Locate every Plasmodium falciparum-infected red blood cell.
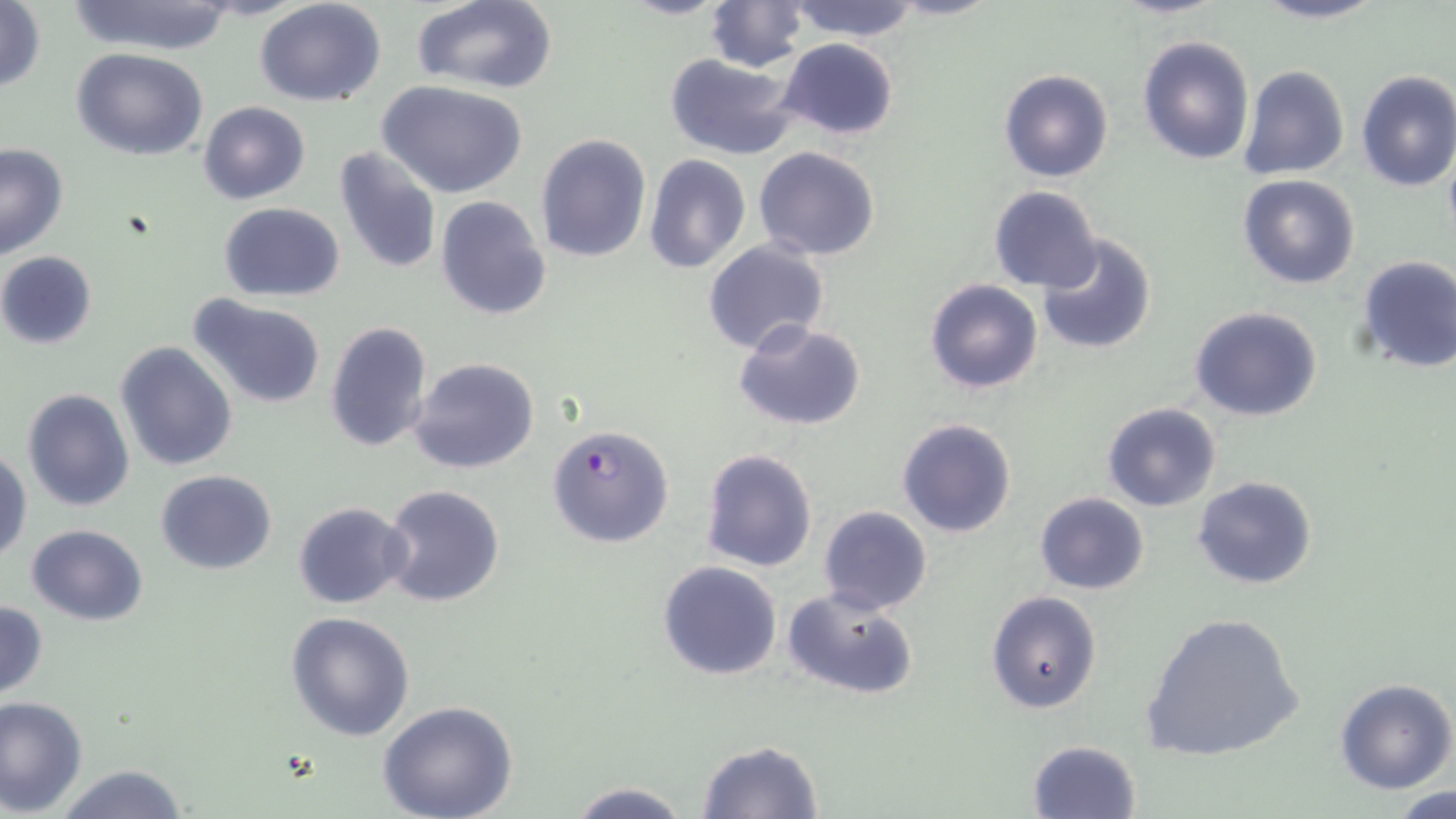

Approximate bounding boxes as named x1/y1/x2/y2 corners in pixels.
Plasmodium falciparum-infected red blood cells: (x1=547, y1=424, x2=675, y2=548).

Summary:
  - Uninfected red blood cell locations: (x1=65, y1=0, x2=241, y2=55), (x1=253, y1=0, x2=387, y2=107), (x1=410, y1=0, x2=559, y2=93), (x1=618, y1=0, x2=731, y2=19), (x1=787, y1=0, x2=922, y2=41), (x1=1113, y1=0, x2=1226, y2=19), (x1=1251, y1=0, x2=1387, y2=25), (x1=1, y1=1, x2=48, y2=94), (x1=704, y1=1, x2=809, y2=72), (x1=1137, y1=34, x2=1255, y2=167), (x1=777, y1=38, x2=901, y2=142), (x1=71, y1=47, x2=210, y2=161), (x1=664, y1=53, x2=803, y2=161), (x1=1238, y1=65, x2=1350, y2=181), (x1=998, y1=68, x2=1114, y2=184), (x1=1354, y1=69, x2=1456, y2=192), (x1=378, y1=80, x2=528, y2=198), (x1=198, y1=100, x2=310, y2=204), (x1=535, y1=132, x2=652, y2=263), (x1=0, y1=144, x2=69, y2=261), (x1=332, y1=144, x2=442, y2=276), (x1=753, y1=147, x2=881, y2=261), (x1=644, y1=155, x2=750, y2=274), (x1=1239, y1=175, x2=1361, y2=290), (x1=988, y1=185, x2=1104, y2=293), (x1=433, y1=196, x2=552, y2=321), (x1=218, y1=202, x2=345, y2=300), (x1=1034, y1=233, x2=1159, y2=356), (x1=702, y1=239, x2=830, y2=357), (x1=0, y1=251, x2=98, y2=350), (x1=1355, y1=254, x2=1456, y2=375), (x1=924, y1=279, x2=1044, y2=395), (x1=187, y1=292, x2=328, y2=410), (x1=1190, y1=306, x2=1323, y2=422), (x1=733, y1=318, x2=867, y2=431), (x1=324, y1=320, x2=434, y2=453), (x1=115, y1=341, x2=237, y2=471), (x1=408, y1=356, x2=541, y2=475), (x1=22, y1=389, x2=135, y2=513), (x1=1101, y1=403, x2=1222, y2=513), (x1=896, y1=417, x2=1017, y2=538), (x1=1, y1=447, x2=32, y2=563), (x1=699, y1=448, x2=818, y2=573), (x1=155, y1=470, x2=278, y2=574), (x1=1192, y1=475, x2=1319, y2=590), (x1=381, y1=484, x2=505, y2=607), (x1=1034, y1=492, x2=1149, y2=595), (x1=292, y1=501, x2=411, y2=608), (x1=818, y1=506, x2=933, y2=615), (x1=26, y1=524, x2=149, y2=624), (x1=657, y1=560, x2=783, y2=681), (x1=780, y1=588, x2=916, y2=702), (x1=987, y1=591, x2=1102, y2=713), (x1=0, y1=599, x2=49, y2=701), (x1=286, y1=610, x2=416, y2=741), (x1=1141, y1=612, x2=1307, y2=763), (x1=1333, y1=678, x2=1456, y2=794), (x1=0, y1=696, x2=88, y2=816), (x1=377, y1=700, x2=519, y2=819), (x1=696, y1=740, x2=824, y2=819), (x1=1028, y1=740, x2=1141, y2=818), (x1=51, y1=764, x2=191, y2=819), (x1=563, y1=780, x2=692, y2=818), (x1=1387, y1=787, x2=1456, y2=819)
  - Slide-level diagnosis: Plasmodium falciparum
  - Stain: May-Grünwald-Giemsa
  - Image size: 1456×819 pixels
  - Preparation: thin blood film
  - Modality: light microscopy
  - Magnification: 1000x
  - Field of view: one of a larger specimen